State which parasite is depicted.
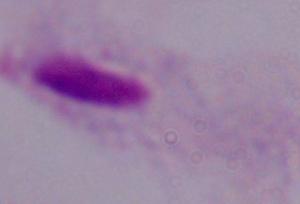

A trichomonad.

Summary:
  - Magnification: 1000x
  - Modality: micrograph